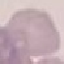
malaria_status: uninfected
preparation: thin blood film
capture: smartphone camera at the microscope eyepiece
stain: Giemsa
image_type: cell patch, automatically extracted from a larger field of view and resized to 64 × 64 pixels